Locate malaria parasites and leukocytes.
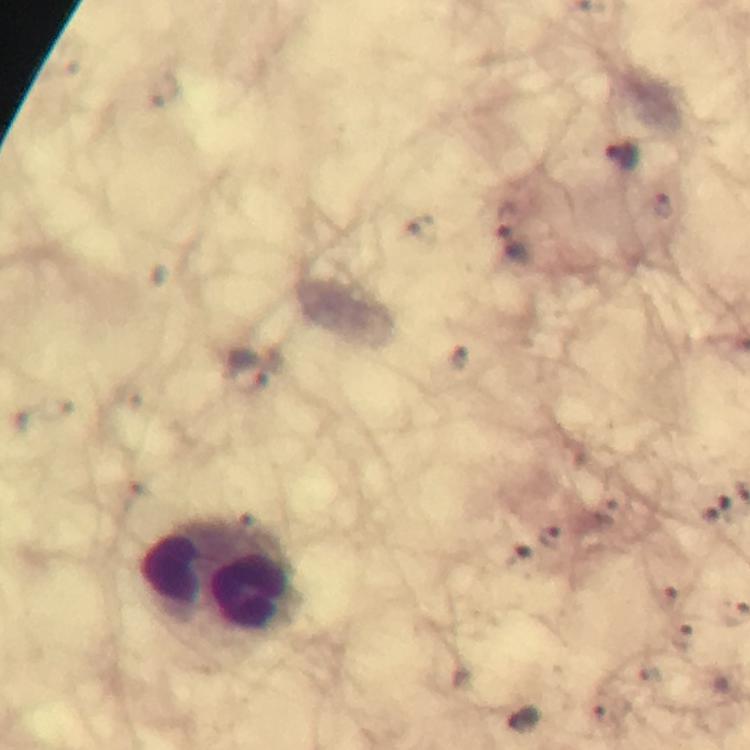

Approximate centers as [x, y] in pixels.
Malaria parasites: [624, 155], [663, 207], [511, 245], [247, 373], [551, 537].
Leukocytes: [171, 567], [255, 574].

magnification = 100x
capture = smartphone photograph through a microscope
immersion oil = applied
cropped from = a single field of view
preparation = thick blood smear
image size = 750×750 pixels
stain = Giemsa
context = from a diagnostic examination for malaria